Locate every blood parasite and identify its species.
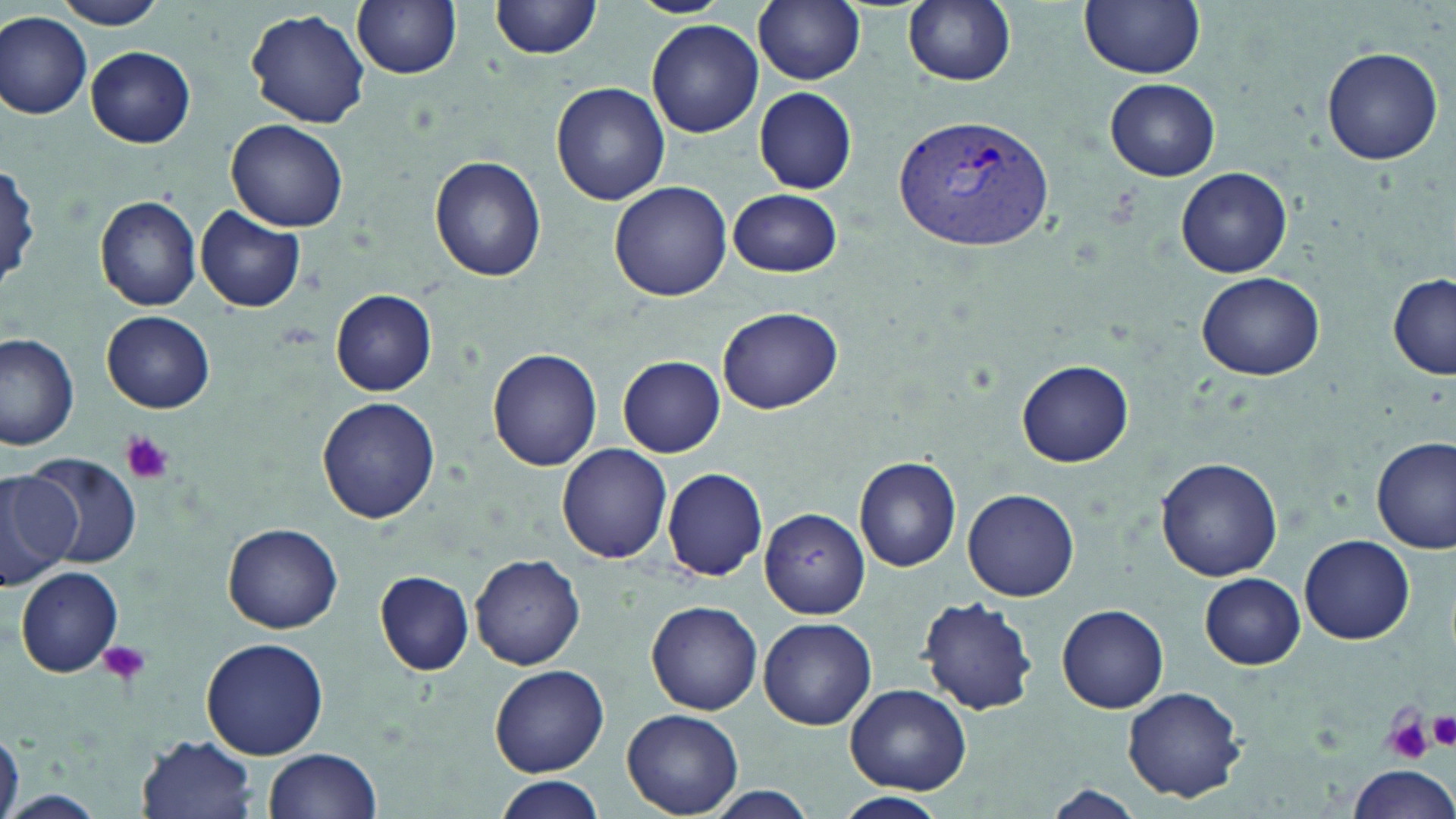

Approximate bounding boxes as named x1/y1/x2/y2 corners in pixels.
Plasmodium vivax-infected red blood cells: (x1=893, y1=113, x2=1058, y2=252).
No Plasmodium falciparum, Plasmodium ovale, Plasmodium malariae, Babesia divergens, or Trypanosoma brucei observed.

Summary:
  - Uninfected red blood cell locations: (x1=50, y1=0, x2=169, y2=28), (x1=352, y1=0, x2=462, y2=80), (x1=490, y1=0, x2=605, y2=61), (x1=628, y1=0, x2=729, y2=17), (x1=752, y1=0, x2=865, y2=86), (x1=902, y1=0, x2=1016, y2=87), (x1=1080, y1=0, x2=1206, y2=78), (x1=245, y1=8, x2=371, y2=130), (x1=0, y1=11, x2=92, y2=121), (x1=646, y1=20, x2=763, y2=137), (x1=86, y1=45, x2=196, y2=148), (x1=1321, y1=46, x2=1444, y2=167), (x1=1104, y1=77, x2=1220, y2=181), (x1=551, y1=82, x2=670, y2=206), (x1=754, y1=88, x2=858, y2=194), (x1=227, y1=120, x2=349, y2=232), (x1=429, y1=156, x2=546, y2=283), (x1=0, y1=165, x2=44, y2=292), (x1=1175, y1=167, x2=1293, y2=277), (x1=608, y1=180, x2=732, y2=302), (x1=728, y1=189, x2=842, y2=277), (x1=96, y1=195, x2=203, y2=311), (x1=195, y1=207, x2=305, y2=312), (x1=1197, y1=271, x2=1326, y2=381), (x1=1387, y1=275, x2=1456, y2=379), (x1=332, y1=291, x2=437, y2=394), (x1=719, y1=306, x2=842, y2=414), (x1=103, y1=311, x2=216, y2=413), (x1=0, y1=333, x2=80, y2=451), (x1=487, y1=350, x2=603, y2=473), (x1=617, y1=356, x2=725, y2=457), (x1=1017, y1=358, x2=1133, y2=466), (x1=316, y1=397, x2=440, y2=523), (x1=1372, y1=435, x2=1455, y2=554), (x1=557, y1=444, x2=673, y2=564), (x1=28, y1=455, x2=142, y2=567), (x1=854, y1=457, x2=962, y2=572), (x1=1156, y1=458, x2=1282, y2=581), (x1=662, y1=466, x2=770, y2=581), (x1=0, y1=467, x2=82, y2=585), (x1=962, y1=488, x2=1081, y2=603), (x1=759, y1=505, x2=871, y2=619), (x1=223, y1=524, x2=343, y2=634), (x1=1298, y1=535, x2=1414, y2=645), (x1=471, y1=554, x2=586, y2=670), (x1=14, y1=567, x2=123, y2=678), (x1=374, y1=571, x2=475, y2=675), (x1=1198, y1=572, x2=1306, y2=669), (x1=917, y1=591, x2=1039, y2=713), (x1=645, y1=601, x2=763, y2=716), (x1=1057, y1=605, x2=1170, y2=714), (x1=757, y1=616, x2=876, y2=731), (x1=199, y1=638, x2=329, y2=759), (x1=489, y1=664, x2=609, y2=776), (x1=843, y1=683, x2=972, y2=793), (x1=1122, y1=686, x2=1248, y2=804), (x1=624, y1=709, x2=742, y2=816), (x1=0, y1=728, x2=23, y2=819), (x1=137, y1=733, x2=260, y2=818), (x1=264, y1=748, x2=383, y2=819), (x1=1348, y1=763, x2=1456, y2=818), (x1=492, y1=776, x2=607, y2=819), (x1=1042, y1=784, x2=1145, y2=819), (x1=699, y1=789, x2=824, y2=819), (x1=0, y1=790, x2=107, y2=818), (x1=833, y1=791, x2=949, y2=818)
  - Platelet locations: (x1=119, y1=432, x2=174, y2=485), (x1=100, y1=639, x2=150, y2=689), (x1=1426, y1=710, x2=1456, y2=751), (x1=1385, y1=714, x2=1435, y2=765)
  - Slide-level diagnosis: Plasmodium vivax
  - Modality: optical microscopy
  - Field of view: one of a larger specimen
  - Stain: May-Grünwald-Giemsa
  - Magnification: 1000x
  - Image size: 1456×819 pixels
  - Preparation: thin blood smear